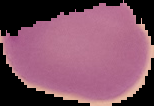 Malaria status: uninfected. From a thin blood film. Image is 154×106 pixels. Cell region segmented out of the field of view; the surrounding area is masked to black.